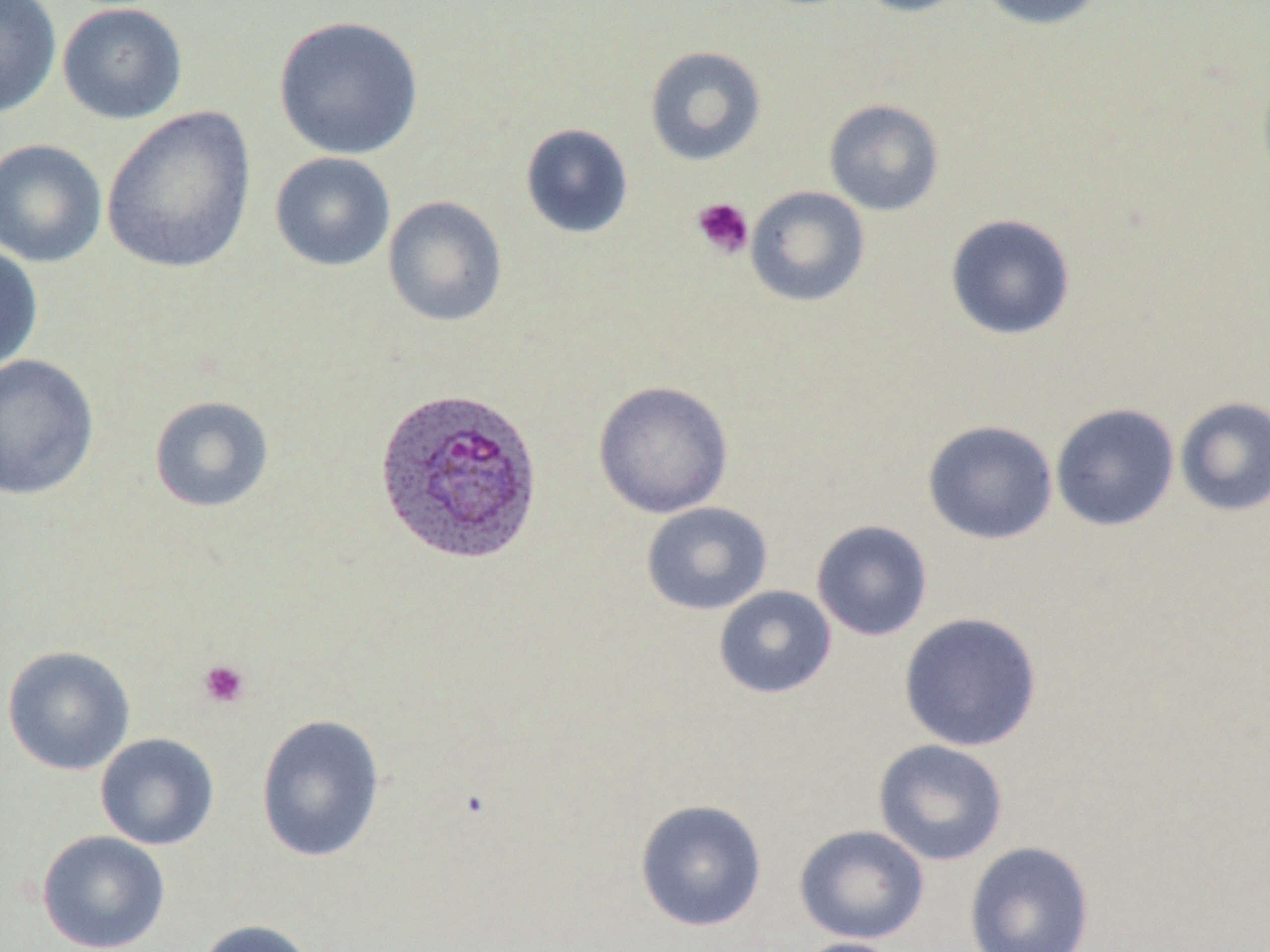
Summary:
  - Coordinate format: approximate bounding boxes as [x1, y1, x2, y2] in pixels
  - Uninfected red blood cell locations: [0, 0, 62, 119], [852, 0, 974, 17], [975, 0, 1108, 30], [57, 2, 188, 124], [273, 15, 424, 160], [644, 45, 766, 166], [823, 98, 945, 216], [101, 105, 256, 274], [519, 123, 634, 239], [0, 138, 107, 267], [269, 151, 395, 272], [745, 186, 869, 307], [382, 195, 508, 327], [944, 213, 1076, 340], [0, 243, 44, 375], [0, 353, 99, 500], [593, 380, 734, 518], [149, 395, 274, 512], [1175, 397, 1270, 516], [1050, 403, 1180, 531], [922, 419, 1058, 544], [640, 501, 773, 615], [811, 519, 933, 641], [713, 585, 837, 699], [898, 611, 1043, 752], [1, 645, 135, 775], [256, 714, 386, 863], [95, 733, 219, 850], [872, 738, 1009, 866], [634, 798, 768, 932], [794, 824, 930, 944], [36, 830, 171, 952], [964, 840, 1095, 952], [195, 919, 318, 952], [788, 937, 906, 952]
  - Plasmodium ovale-infected red blood cell locations: [372, 386, 545, 565]
  - Platelet locations: [691, 196, 754, 259], [198, 659, 250, 709]
  - Slide-level diagnosis: Plasmodium ovale
  - Field of view: one of a larger specimen
  - Magnification: 1000x
  - Preparation: thin blood smear
  - Image size: 1270×952 pixels
  - Stain: May-Grünwald-Giemsa
  - Modality: optical microscopy